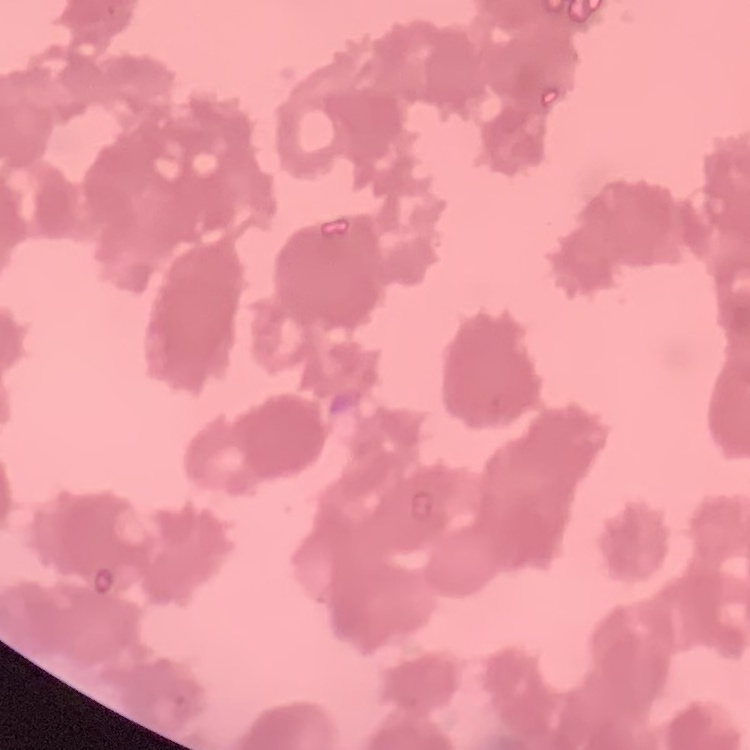
{
  "red_blood_cell_morphology": "rouleaux formation",
  "preparation": "thin blood film",
  "image_type": "square crop of a larger photomicrograph",
  "stain": "Field's or Giemsa"
}